Comment on the morphology of the erythrocytes.
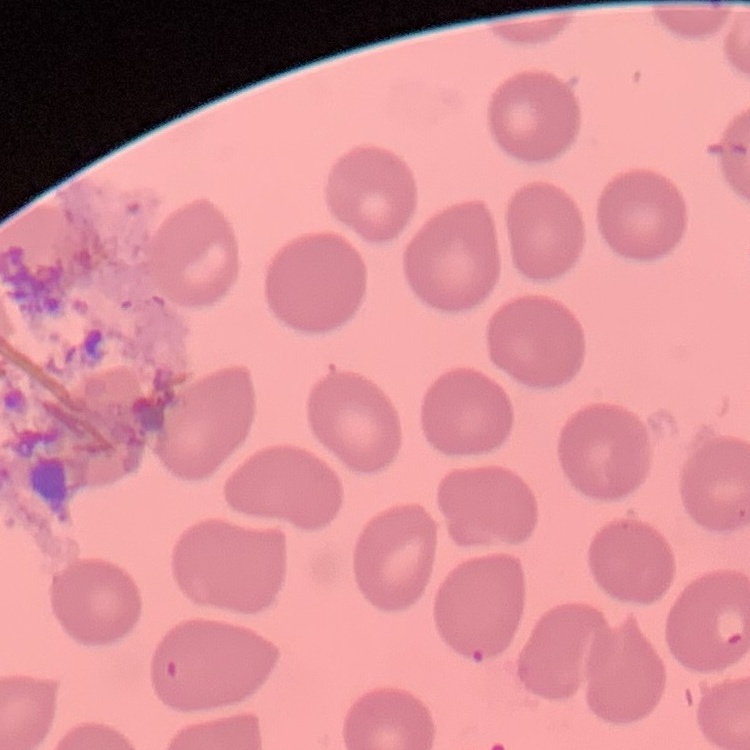
They show no rouleaux formation.

Summary:
  - Stain: Field's or Giemsa
  - Preparation: thin blood smear
  - Image type: square crop of a larger photomicrograph